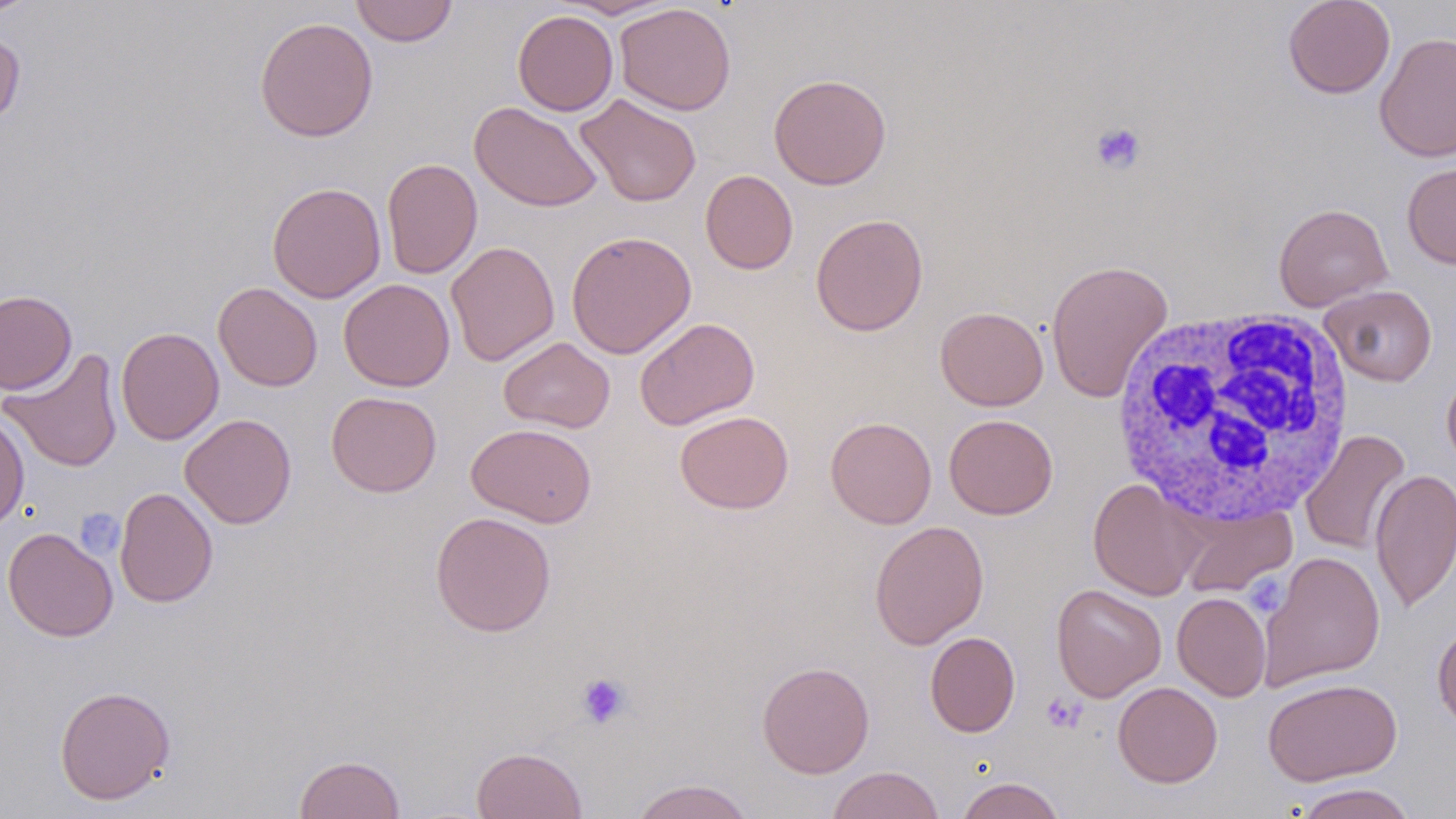
slide_level_diagnosis: no evidence of blood parasites
preparation: thin blood smear
uninfected_red_blood_cell_locations: 'approximate bounding boxes as (x1,y1)-(x2,y2) corner pairs in pixels: (0,0)-(42,20), (350,0)-(457,46), (554,0)-(678,19), (1282,0)-(1396,99), (615,3)-(736,115), (513,10)-(618,116), (255,16)-(379,142), (0,30)-(25,130), (1374,32)-(1456,163), (769,73)-(892,189), (576,93)-(701,207), (470,101)-(602,212), (382,157)-(483,279), (1401,162)-(1456,269), (700,169)-(799,274), (267,182)-(386,303), (1273,203)-(1393,311), (810,213)-(928,336), (566,230)-(697,359), (445,241)-(560,366), (1046,259)-(1173,404), (338,278)-(455,391), (213,282)-(322,391), (1319,284)-(1438,386), (0,290)-(77,395), (935,306)-(1048,410), (633,317)-(760,430), (116,326)-(224,445), (499,337)-(615,433), (1,348)-(123,473), (1442,369)-(1456,472), (326,391)-(441,497), (675,410)-(794,514), (0,411)-(30,532), (179,413)-(297,529), (944,414)-(1058,519), (825,416)-(937,529), (466,422)-(596,528), (1300,430)-(1411,555), (1370,468)-(1456,613), (1087,478)-(1204,600), (115,487)-(218,608), (1175,503)-(1297,597), (430,511)-(556,637), (869,520)-(989,649), (2,527)-(118,642), (1259,551)-(1385,690), (1051,583)-(1167,702), (1172,592)-(1271,701), (1432,622)-(1456,732), (924,631)-(1020,737), (756,661)-(875,778), (1262,677)-(1402,786), (1113,681)-(1223,787), (54,685)-(176,805), (471,746)-(588,819), (294,754)-(406,818), (827,766)-(945,819), (955,776)-(1068,819), (629,778)-(756,819), (1291,783)-(1418,819)'
magnification: 1000x
white_blood_cell_locations: 'approximate bounding boxes as (x1,y1)-(x2,y2) corner pairs in pixels: (1106,307)-(1357,530)'
platelet_locations: 'approximate bounding boxes as (x1,y1)-(x2,y2) corner pairs in pixels: (1089,121)-(1147,176), (75,508)-(124,558), (1252,571)-(1290,613), (575,672)-(631,729), (1041,692)-(1086,733)'
modality: light microscopy
image_size: 1456×819 pixels
field_of_view: one of a larger specimen
stain: May-Grünwald-Giemsa